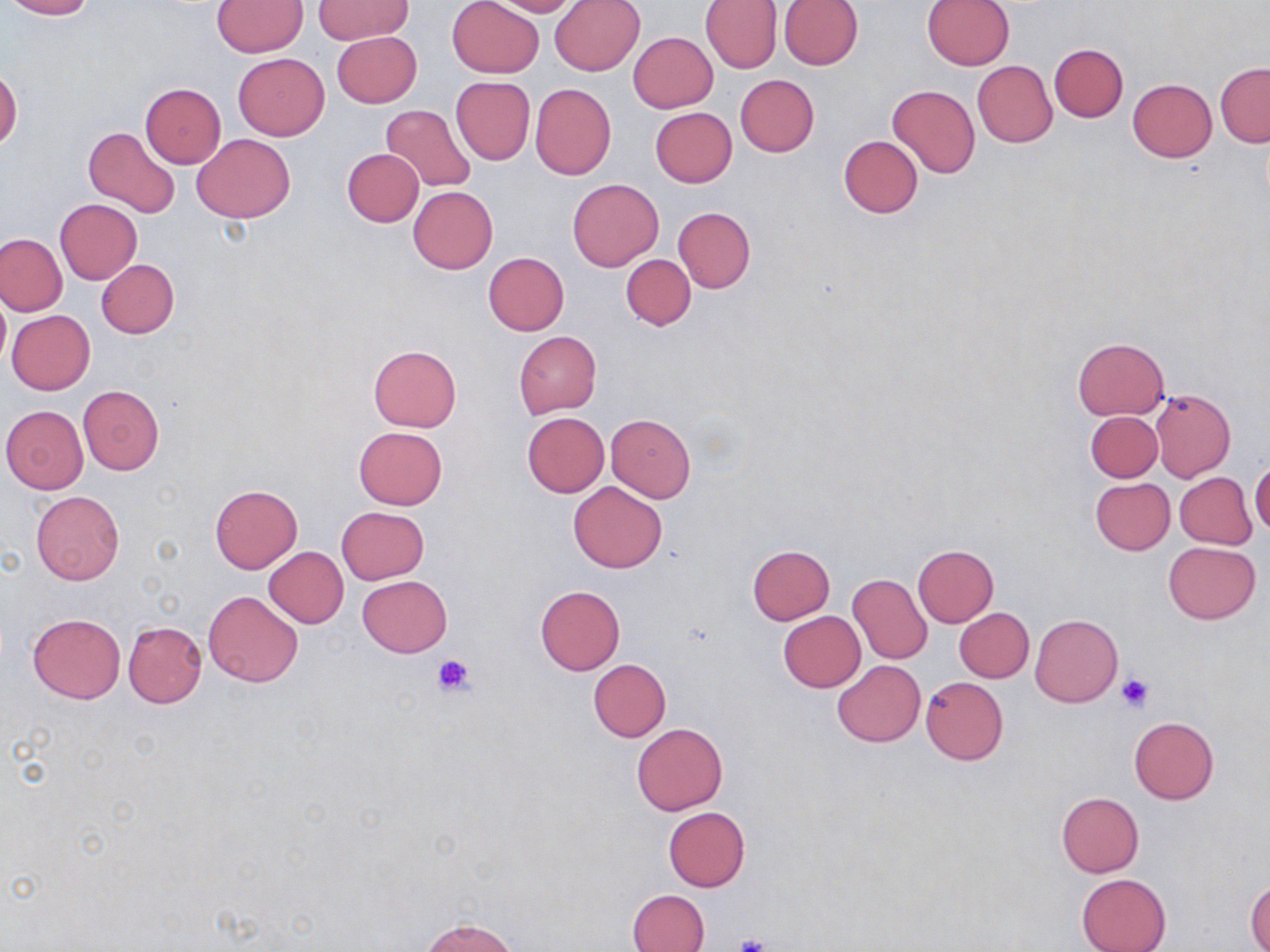
Approximate bounding boxes as (x1, y1, x2, y2) in pixels. Uninfected red blood cell locations: (3, 0, 96, 19), (448, 0, 544, 78), (482, 0, 583, 16), (549, 0, 646, 76), (700, 0, 781, 73), (778, 0, 862, 69), (213, 1, 306, 55), (314, 1, 411, 44), (922, 1, 1014, 70), (332, 30, 422, 107), (628, 32, 717, 112), (1049, 43, 1128, 121), (233, 53, 330, 141), (972, 61, 1057, 147), (1215, 62, 1269, 147), (0, 66, 21, 150), (734, 74, 819, 157), (450, 77, 536, 166), (1126, 79, 1217, 162), (531, 82, 616, 180), (139, 83, 226, 167), (887, 84, 979, 179), (381, 105, 476, 192), (650, 107, 736, 187), (84, 125, 179, 217), (193, 134, 295, 223), (838, 135, 923, 217), (343, 149, 423, 226), (567, 178, 663, 272), (409, 186, 498, 272), (55, 199, 142, 283), (672, 207, 756, 293), (0, 232, 67, 315), (482, 252, 570, 335), (621, 254, 696, 330), (96, 259, 179, 338), (0, 291, 9, 373), (6, 310, 95, 394), (513, 332, 602, 419), (1073, 337, 1169, 419), (368, 344, 462, 432), (77, 385, 165, 475), (1151, 389, 1236, 482), (1, 405, 88, 493), (1086, 411, 1162, 481), (522, 412, 609, 496), (607, 414, 695, 501), (353, 426, 447, 510), (1249, 461, 1270, 535), (1174, 472, 1257, 549), (1090, 478, 1174, 554), (568, 482, 668, 573), (209, 485, 302, 573), (31, 491, 124, 584), (337, 505, 430, 585), (1163, 541, 1260, 623), (747, 544, 835, 625), (912, 544, 998, 626), (264, 547, 348, 627), (849, 574, 932, 663), (357, 575, 453, 657), (535, 585, 624, 675), (203, 590, 302, 687), (954, 607, 1034, 682), (779, 612, 865, 692), (27, 613, 125, 704), (1029, 615, 1123, 707), (123, 621, 206, 707), (589, 659, 671, 743), (832, 660, 924, 747), (921, 676, 1008, 764), (1128, 716, 1219, 803), (632, 722, 727, 815), (1055, 792, 1144, 877), (662, 807, 750, 892), (1076, 874, 1171, 952), (1246, 878, 1270, 951), (628, 890, 708, 952), (421, 917, 520, 952). Platelet locations: (432, 654, 476, 698), (1117, 674, 1153, 711), (729, 935, 770, 952). Slide-level diagnosis: no evidence of blood parasites. Image is 1270×952 pixels. Optical microscopy. Captured at 1000x magnification. May-Grünwald-Giemsa stain. Thin blood smear. One field of a larger specimen.